Report the malaria status of this cell.
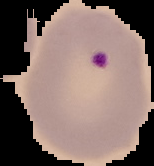
It is parasitized.

From a thin blood smear. Image is 154×166 pixels. Cell region segmented out of the field of view; the surrounding area is masked to black.